Assess this cell for malaria.
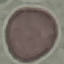
Uninfected.

Summary:
  - Preparation: thin smear
  - Capture: smartphone through the microscope eyepiece
  - Stain: Giemsa
  - Image type: cell patch, automatically extracted from a larger field of view and resized to 64 × 64 pixels